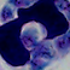 Captured at 1000x magnification. A white blood cell is seen. Micrograph.